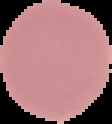
{
  "preparation": "thin blood film",
  "result": "no malaria parasites seen",
  "image_type": "segmented cell region with the area outside set to black",
  "image_size": "112×124 pixels"
}